Give the position of every Plasmodium parasite.
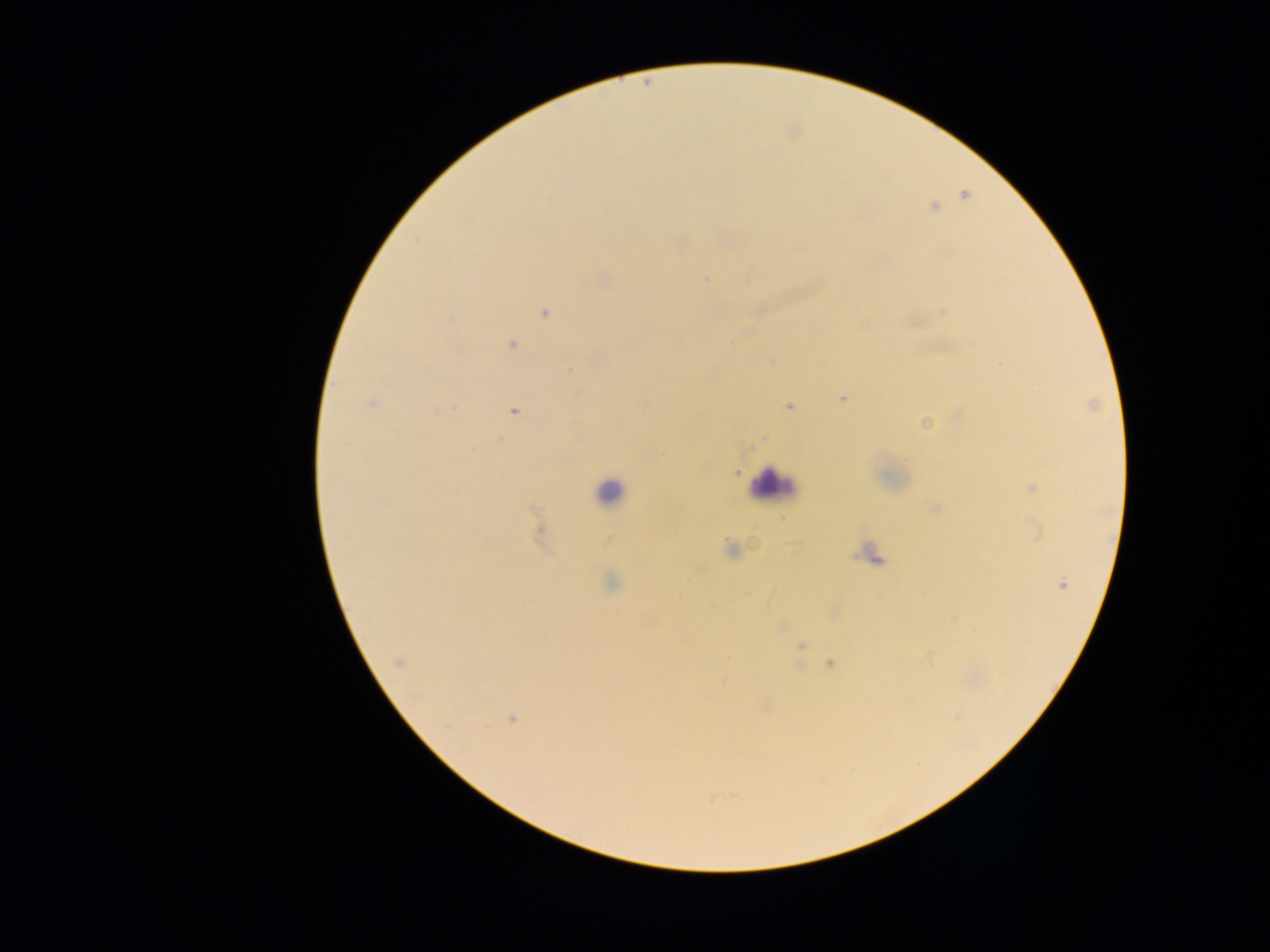

Approximate centers as (x, y) in pixels.
Plasmodium parasites: (964, 194), (934, 206), (678, 245), (706, 280), (759, 309), (943, 311), (544, 312), (511, 344), (771, 361), (569, 370), (844, 398), (373, 404), (788, 407), (437, 410), (514, 410), (958, 415), (924, 423), (763, 439), (703, 466), (736, 472), (1030, 487), (935, 509), (540, 530), (729, 549), (612, 582), (1061, 584), (834, 611), (781, 627), (801, 645), (398, 662), (831, 662), (766, 705), (511, 719).

Summary:
  - Leukocyte locations: (771, 485), (609, 491), (870, 553)
  - Capture: mobile-phone photograph through a microscope
  - Field of view: single
  - Image size: 1270×952 pixels
  - Country: Ghana
  - Preparation: thick blood film